State which parasite is depicted.
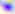
Toxoplasma gondii.

Summary:
  - Modality: micrograph
  - Magnification: 400x